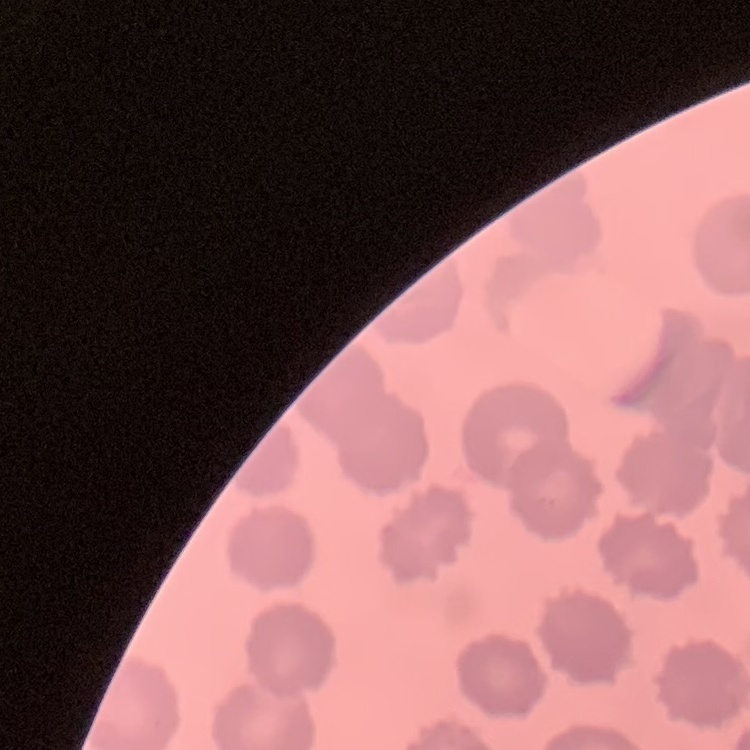

red blood cell morphology = no rouleaux formation
image type = one tile cut from a larger photomicrograph
preparation = thin blood film
stain = Field's or Giemsa